Give the location of every parasitized red blood cell.
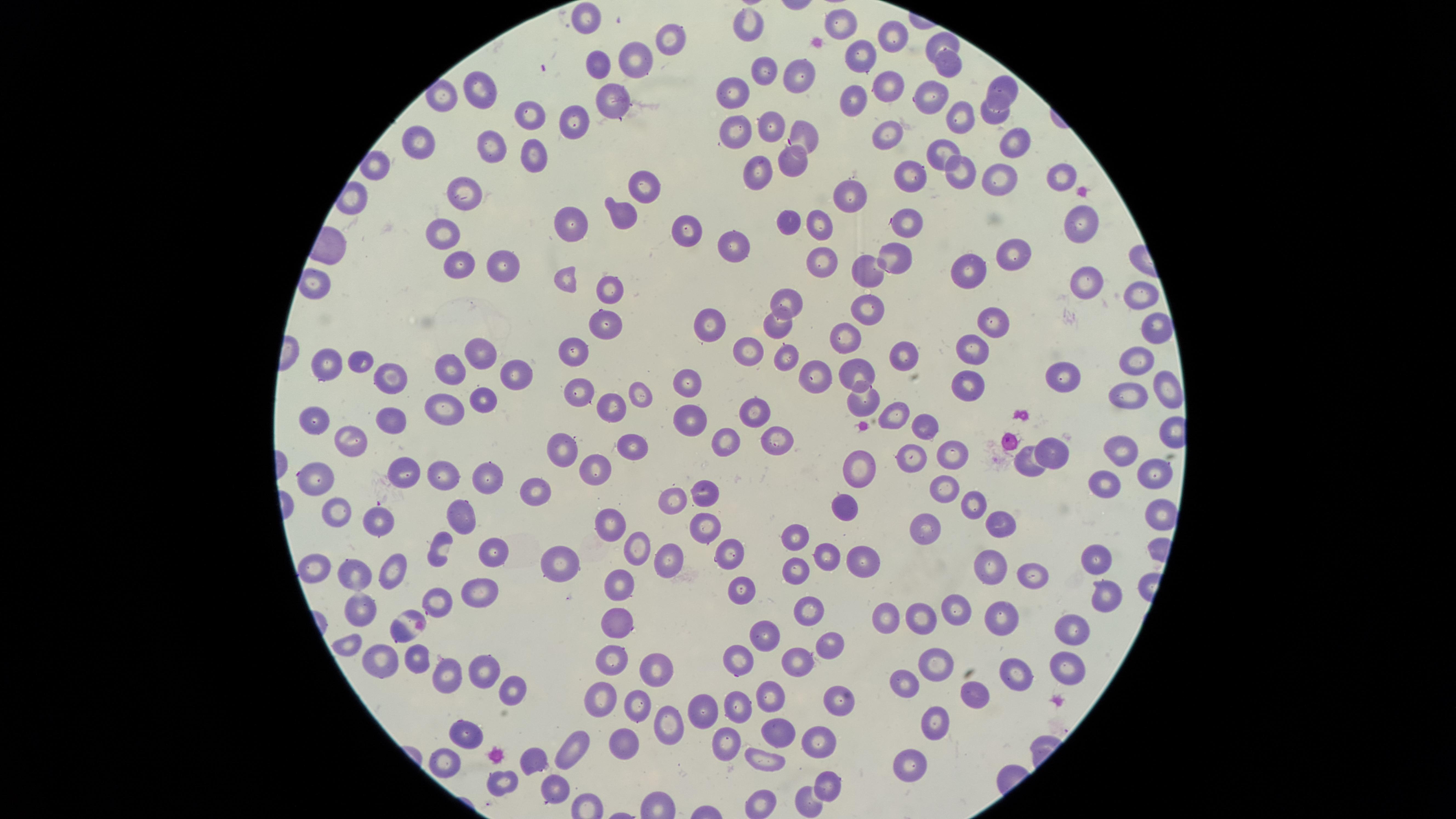

No parasitized red blood cells identified.

visible_region: circular
uninfected_red_blood_cells: 'approximate marker points as {x, y} in pixels: {590, 12}, {750, 22}, {839, 26}, {892, 33}, {670, 38}, {944, 42}, {632, 58}, {865, 60}, {946, 60}, {595, 68}, {765, 68}, {798, 77}, {482, 85}, {887, 87}, {1002, 87}, {933, 95}, {732, 96}, {857, 100}, {445, 102}, {612, 107}, {997, 110}, {538, 111}, {578, 119}, {966, 119}, {773, 125}, {800, 132}, {737, 134}, {888, 134}, {1016, 138}, {492, 146}, {417, 149}, {936, 151}, {527, 155}, {793, 160}, {960, 169}, {1058, 172}, {758, 174}, {1002, 178}, {910, 182}, {641, 185}, {465, 190}, {849, 195}, {617, 214}, {789, 217}, {1080, 221}, {569, 224}, {822, 226}, {908, 226}, {688, 227}, {447, 236}, {731, 247}, {1012, 252}, {898, 253}, {821, 263}, {502, 264}, {975, 264}, {463, 266}, {865, 272}, {568, 277}, {1084, 279}, {1145, 288}, {609, 290}, {785, 302}, {866, 306}, {706, 318}, {991, 318}, {602, 323}, {778, 324}, {1157, 326}, {843, 336}, {749, 346}, {970, 347}, {482, 353}, {901, 355}, {569, 359}, {785, 360}, {360, 361}, {1143, 362}, {327, 364}, {451, 371}, {860, 371}, {390, 374}, {1071, 374}, {509, 375}, {821, 377}, {687, 379}, {969, 383}, {1168, 387}, {638, 389}, {1130, 391}, {582, 393}, {480, 400}, {861, 401}, {609, 403}, {446, 405}, {754, 409}, {683, 411}, {898, 413}, {316, 417}, {390, 419}, {923, 427}, {780, 437}, {727, 438}, {348, 441}, {636, 446}, {564, 447}, {1124, 447}, {1055, 449}, {953, 454}, {913, 456}, {1027, 463}, {862, 466}, {593, 469}, {1151, 470}, {443, 472}, {398, 473}, {322, 477}, {488, 477}, {1107, 479}, {943, 486}, {706, 488}, {538, 494}, {676, 499}, {979, 506}, {335, 509}, {460, 510}, {839, 513}, {1160, 514}, {379, 519}, {999, 524}, {613, 525}, {704, 525}, {929, 526}, {797, 534}, {635, 546}, {441, 547}, {493, 548}, {729, 550}, {1098, 553}, {673, 555}, {823, 556}, {562, 563}, {857, 563}, {990, 563}, {320, 567}, {797, 569}, {392, 571}, {1035, 573}, {356, 574}, {623, 583}, {744, 589}, {481, 591}, {1104, 595}, {440, 597}, {961, 602}, {360, 603}, {809, 611}, {1005, 616}, {621, 617}, {893, 617}, {929, 619}, {403, 622}, {1070, 628}, {762, 631}, {831, 642}, {343, 643}, {383, 656}, {938, 657}, {739, 658}, {418, 659}, {799, 662}, {486, 663}, {615, 665}, {1068, 667}, {659, 671}, {1012, 675}, {444, 678}, {901, 680}, {770, 690}, {510, 692}, {972, 693}, {606, 695}, {842, 698}, {637, 701}, {738, 702}, {697, 708}, {932, 719}, {670, 729}, {778, 729}, {463, 731}, {626, 738}, {720, 739}, {818, 739}, {579, 740}, {442, 759}, {532, 759}, {770, 760}, {913, 762}, {829, 780}, {499, 781}, {554, 788}, {808, 799}, {762, 800}'
stain: Giemsa
preparation: thin blood film
capture: smartphone photograph through the microscope eyepiece
image_size: 1456×819 pixels
field_of_view: single